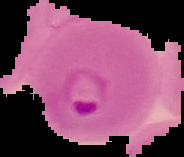
{
  "image_type": "cell region segmented out of the field of view; surrounding area masked to black",
  "malaria_status": "parasitized",
  "preparation": "thin blood smear",
  "image_size": "184×157 pixels"
}